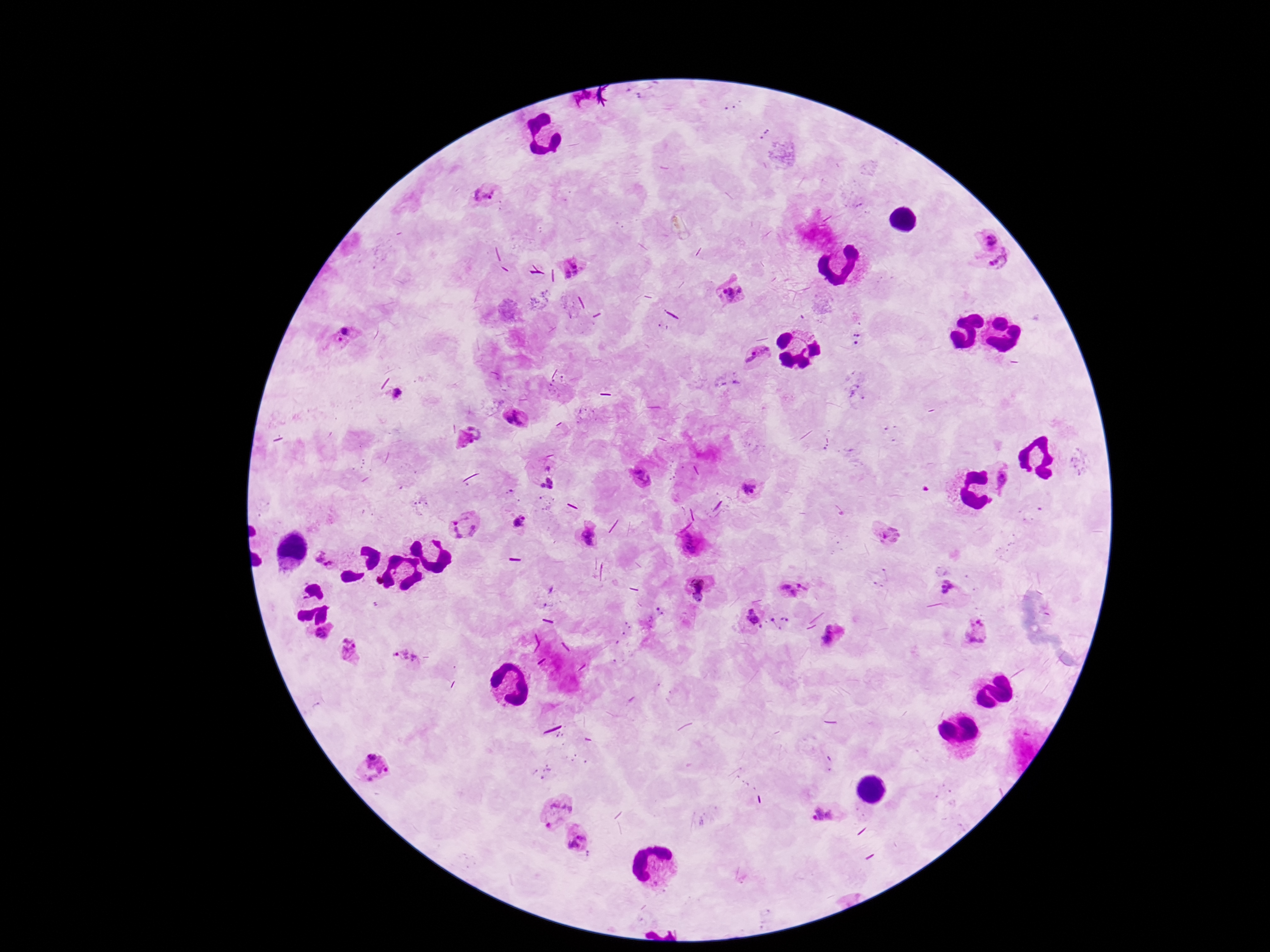
Approximate centers as [x, y] in pixels. Plasmodium parasite locations: [488, 200], [987, 237], [998, 264], [578, 269], [729, 293], [344, 336], [857, 337], [754, 354], [398, 394], [516, 416], [472, 439], [546, 475], [639, 475], [747, 488], [518, 521], [464, 524], [587, 533], [887, 533], [694, 545], [324, 560], [953, 586], [702, 587], [795, 587], [752, 619], [325, 635], [975, 635], [832, 636], [348, 650], [404, 659], [375, 769], [553, 807], [825, 813], [576, 841]. Image is 1270×952 pixels. One field from this slide. Giemsa stain. Smartphone photograph taken through the microscope eyepiece. Patient malaria status: infected. Thick blood film. 100x magnification.